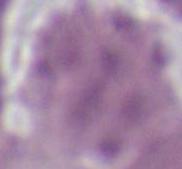

A red blood cell is seen. 1000x magnification. Photomicrograph.